Assess the morphology of the red blood cells.
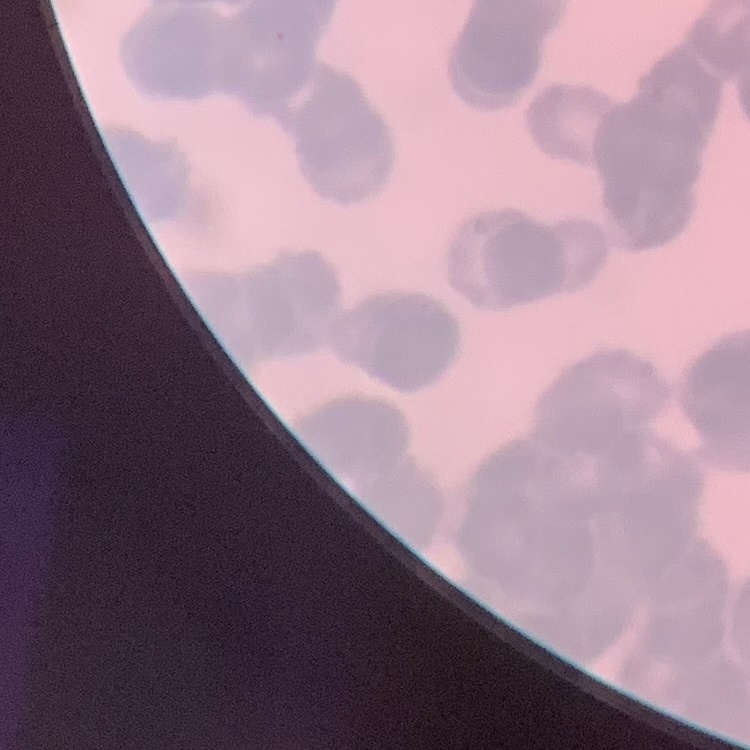
Rouleaux formation.

preparation: thin blood film
stain: Field's or Giemsa
image_type: one tile cut from a larger photomicrograph